Classify the preparation.
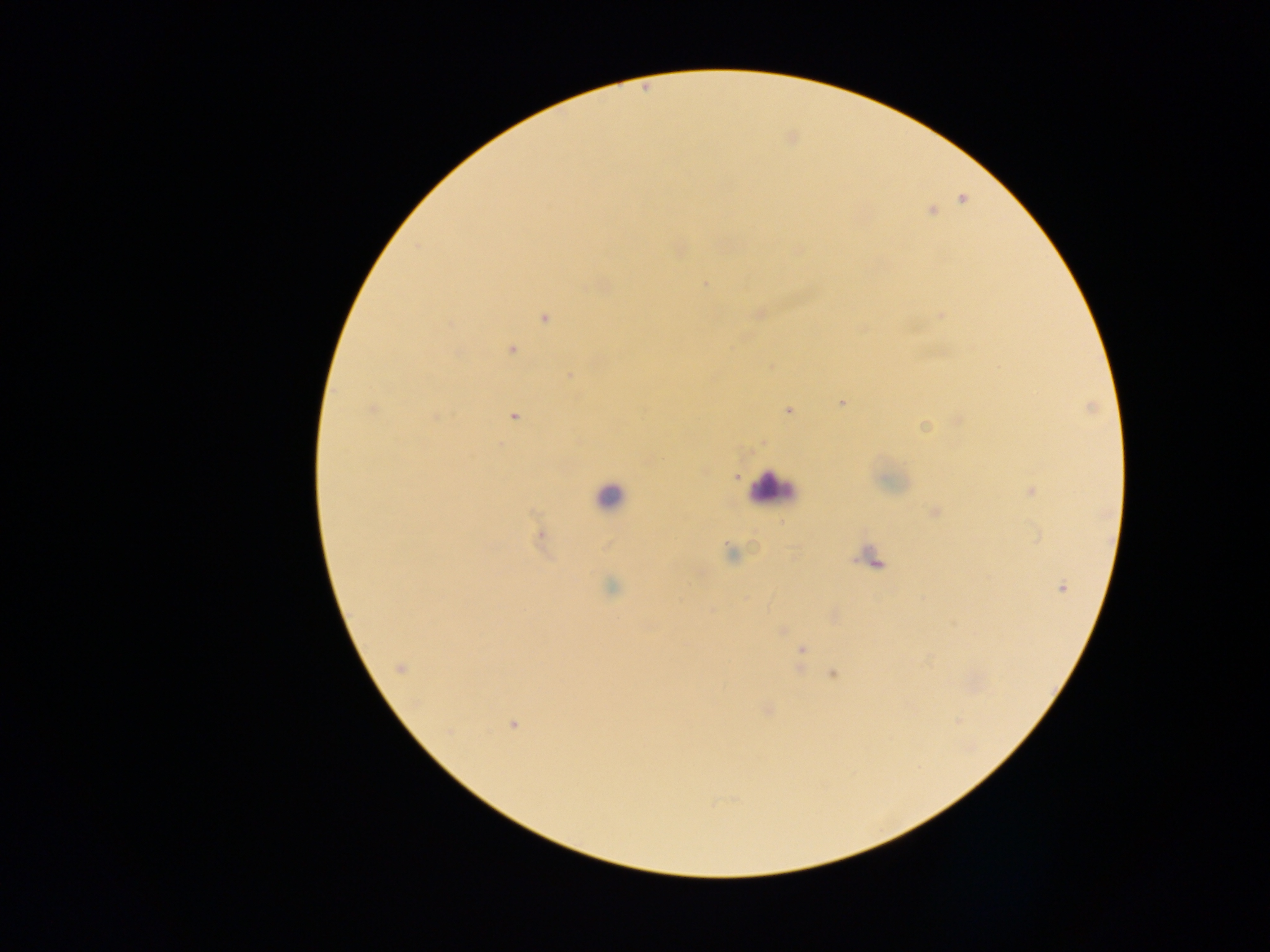

Thick blood smear.

{
  "country": "Ghana",
  "leukocyte_locations": "approximate centers as x y in pixels: 769 488; 608 496",
  "image_size": "1270×952 pixels",
  "field_of_view": "single",
  "malaria_parasite_locations": "approximate centers as x y in pixels: 932 211; 705 284; 940 316; 543 319; 511 350; 771 366; 571 375; 841 403; 371 409; 788 411; 514 416; 959 420; 924 427; 735 477; 1031 491; 935 512; 540 535; 730 553; 612 586; 1062 588; 782 631; 802 650; 400 668; 833 674; 512 725",
  "capture": "mobile-phone photograph through a microscope"
}